Assess this cell for malaria.
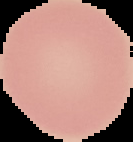

It is uninfected.

image_size: 133×142 pixels
image_type: cell region segmented out of the field of view; surrounding area masked to black
preparation: thin blood film